Assess the morphology of the erythrocytes.
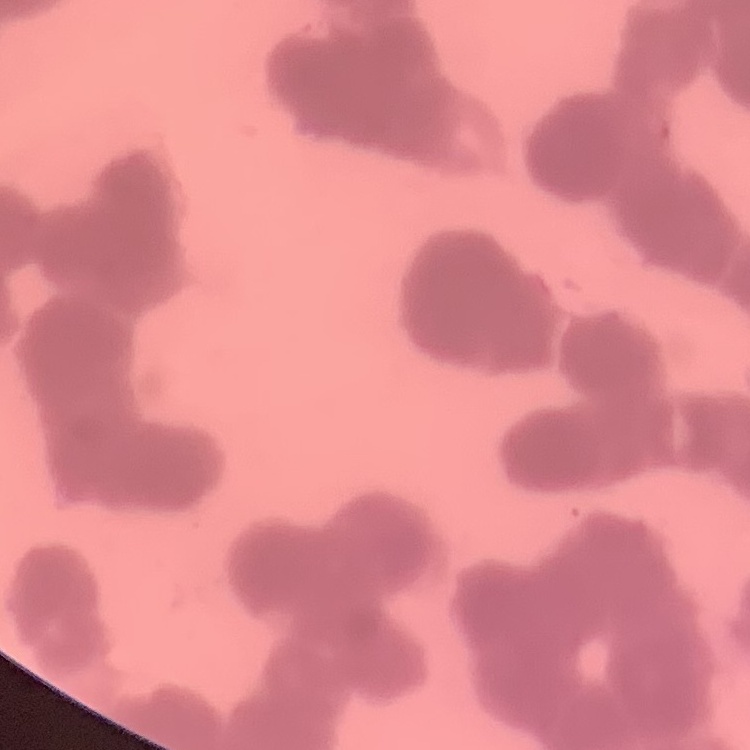
They show rouleaux formation.

Thin peripheral smear. One tile cut from a larger photomicrograph. Field's or Giemsa stain.